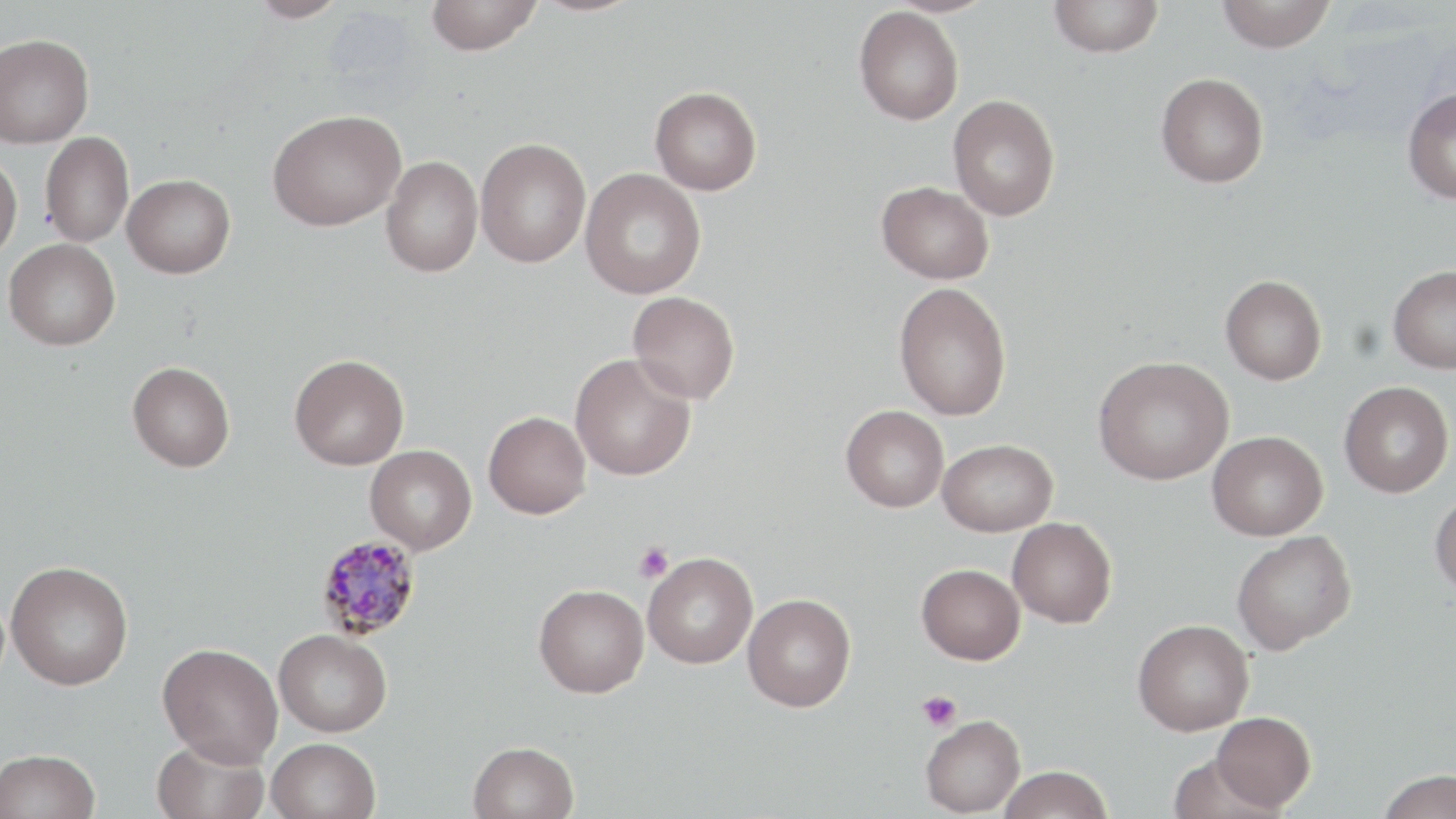

slide-level diagnosis = Plasmodium malariae
field of view = single
magnification = 1000x
stain = May-Grünwald-Giemsa
modality = light microscopy
Plasmodium malariae-infected red blood cell locations = approximate bounding boxes as named x1/y1/x2/y2 corners in pixels: (x1=315, y1=534, x2=423, y2=641)
platelet locations = approximate bounding boxes as named x1/y1/x2/y2 corners in pixels: (x1=635, y1=542, x2=673, y2=582), (x1=916, y1=690, x2=962, y2=732)
uninfected red blood cell locations = approximate bounding boxes as named x1/y1/x2/y2 corners in pixels: (x1=248, y1=0, x2=350, y2=23), (x1=425, y1=0, x2=543, y2=55), (x1=529, y1=0, x2=644, y2=16), (x1=1048, y1=0, x2=1164, y2=57), (x1=1217, y1=0, x2=1336, y2=53), (x1=854, y1=6, x2=964, y2=125), (x1=0, y1=33, x2=94, y2=148), (x1=1155, y1=72, x2=1269, y2=188), (x1=650, y1=86, x2=762, y2=195), (x1=1402, y1=87, x2=1456, y2=204), (x1=948, y1=95, x2=1060, y2=220), (x1=267, y1=109, x2=405, y2=231), (x1=40, y1=131, x2=134, y2=247), (x1=475, y1=138, x2=591, y2=268), (x1=0, y1=153, x2=23, y2=263), (x1=381, y1=156, x2=483, y2=277), (x1=580, y1=169, x2=706, y2=298), (x1=122, y1=174, x2=235, y2=278), (x1=877, y1=180, x2=994, y2=284), (x1=4, y1=239, x2=120, y2=350), (x1=1388, y1=265, x2=1456, y2=373), (x1=1221, y1=274, x2=1327, y2=385), (x1=894, y1=282, x2=1012, y2=421), (x1=628, y1=291, x2=740, y2=404), (x1=570, y1=353, x2=696, y2=481), (x1=290, y1=354, x2=409, y2=470), (x1=1093, y1=356, x2=1233, y2=485), (x1=128, y1=361, x2=235, y2=471), (x1=1339, y1=381, x2=1453, y2=497), (x1=841, y1=405, x2=949, y2=512), (x1=483, y1=411, x2=591, y2=518), (x1=1207, y1=431, x2=1327, y2=541), (x1=938, y1=439, x2=1058, y2=536), (x1=365, y1=445, x2=477, y2=554), (x1=1430, y1=490, x2=1456, y2=599), (x1=1007, y1=517, x2=1117, y2=628), (x1=1231, y1=531, x2=1357, y2=654), (x1=643, y1=551, x2=758, y2=669), (x1=6, y1=561, x2=133, y2=690), (x1=917, y1=563, x2=1025, y2=664), (x1=534, y1=584, x2=649, y2=698), (x1=742, y1=593, x2=856, y2=712), (x1=1133, y1=618, x2=1254, y2=735), (x1=274, y1=629, x2=392, y2=737), (x1=157, y1=642, x2=283, y2=767), (x1=1211, y1=711, x2=1316, y2=811), (x1=921, y1=715, x2=1026, y2=817), (x1=152, y1=737, x2=270, y2=819), (x1=266, y1=737, x2=380, y2=819), (x1=468, y1=741, x2=579, y2=819), (x1=0, y1=749, x2=101, y2=819), (x1=1166, y1=753, x2=1288, y2=819), (x1=998, y1=765, x2=1113, y2=819), (x1=1375, y1=769, x2=1456, y2=819)
preparation = thin blood film
image size = 1456×819 pixels